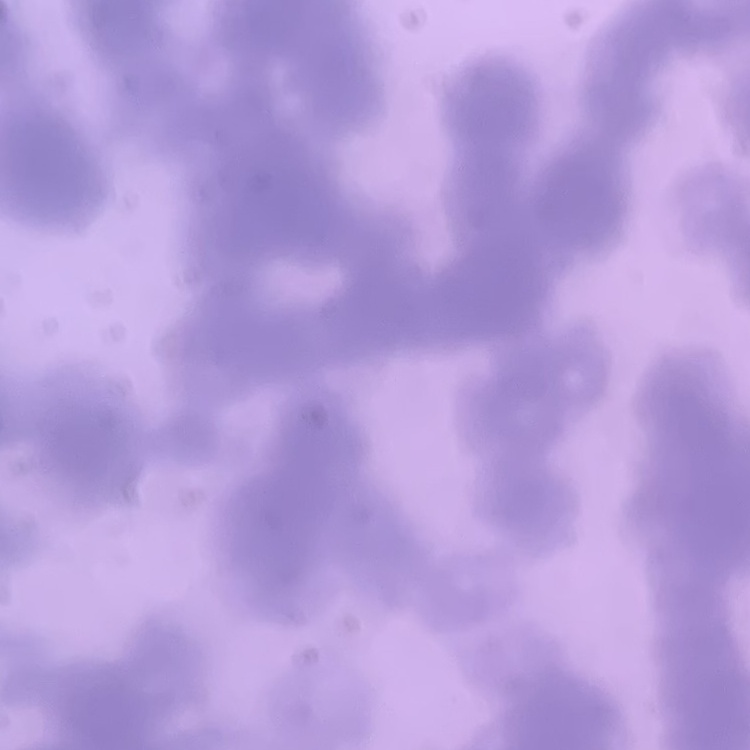

erythrocyte morphology = rouleaux formation
stain = Field's or Giemsa
image type = square crop of a larger photomicrograph
preparation = thin blood smear